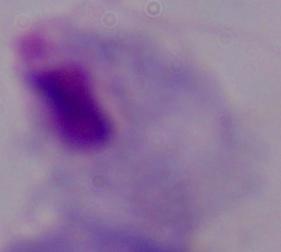

identification = trichomonad
modality = photomicrograph
magnification = 1000x